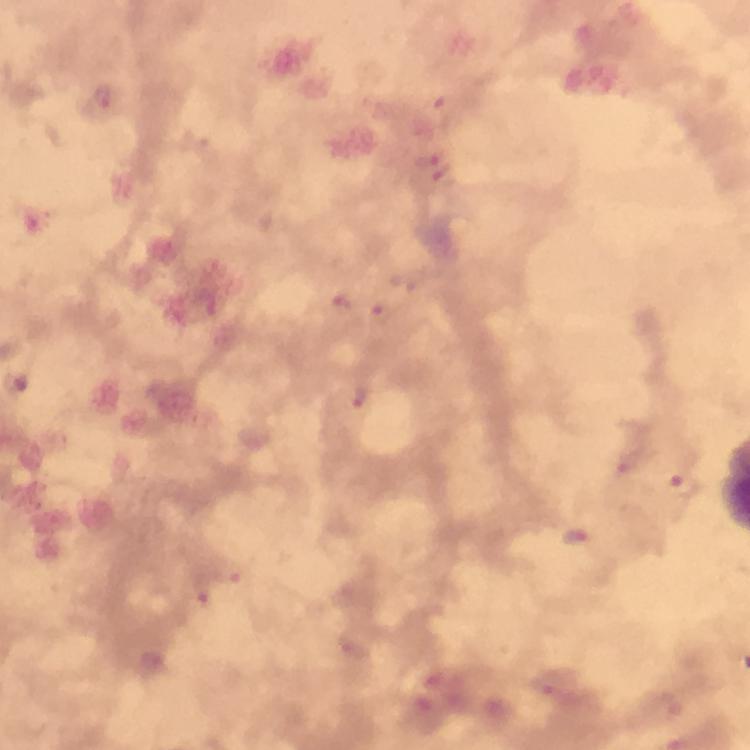

immersion oil = used
stain = Giemsa
magnification = 100x
preparation = thick blood film
cropped from = one field of view
capture = smartphone camera through the microscope
image size = 750×750 pixels
Plasmodium parasite locations = approximate centers as [x, y] in pixels: [426, 160], [434, 179], [402, 281], [342, 303], [379, 314], [17, 385], [360, 396], [683, 486], [574, 538], [230, 573], [201, 595]
context = from a diagnostic examination for malaria